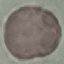
Result: no malaria parasites seen. Thin blood smear. Automatically extracted cell patch, resized to 64 × 64 pixels. Giemsa-stained preparation. Photographed with a smartphone camera at the microscope eyepiece.